Point out leukocytes.
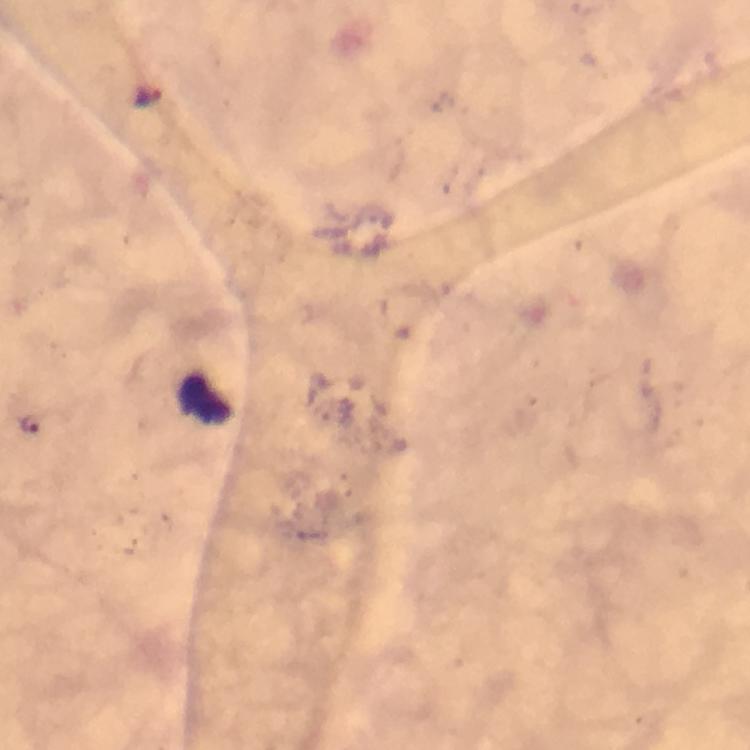

Approximate centers as (x, y) in pixels.
Leukocytes: (205, 399).

Malaria parasite locations: (149, 96), (28, 423). A crop from one field of view. Image is 750×750 pixels. Thick blood film. Immersion oil applied. Giemsa-stained preparation. 100x magnification. From a malaria diagnostic workup. Photographed with a smartphone mounted on the microscope.